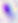

Micrograph. Toxoplasma gondii is seen. Captured at 400x magnification.